Describe the morphology of the red blood cells.
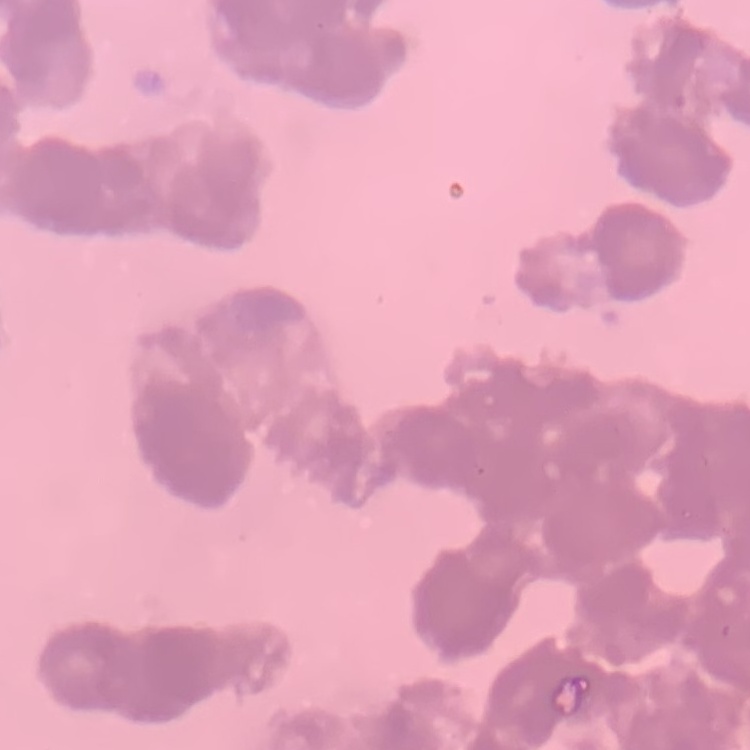
Rouleaux formation.

Thin blood film. Stained with either Field's or Giemsa. One tile cut from a larger photomicrograph.